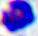
modality = photomicrograph
identification = white blood cell
magnification = 400x